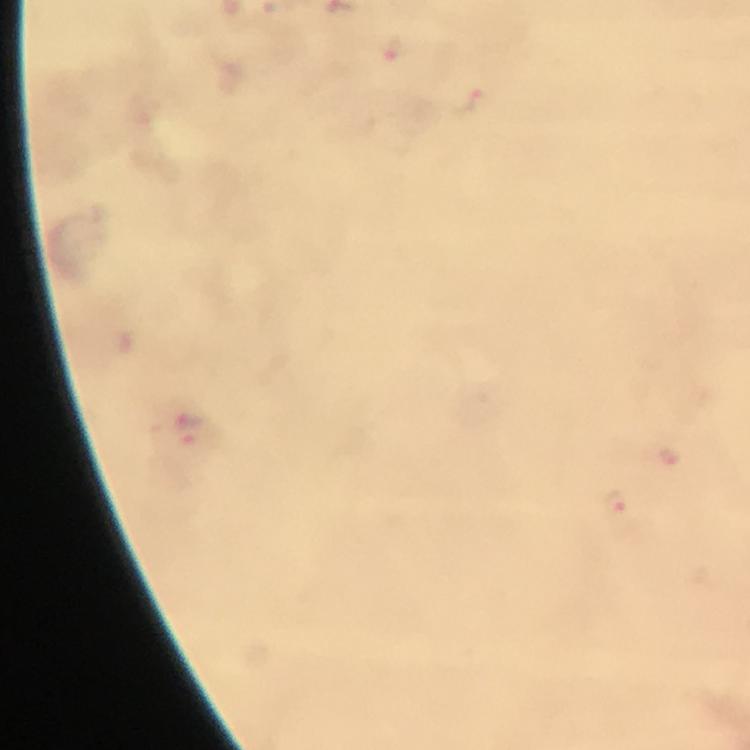

Approximate centers as {x, y} in pixels. Plasmodium parasite locations: {393, 50}, {477, 98}, {190, 432}, {668, 457}, {617, 505}. 100x magnification. Thick blood film. A crop from one field of view. From a diagnostic examination for malaria. Photographed through the microscope with a smartphone camera. Immersion oil applied. Giemsa stain. Image is 750×750 pixels.